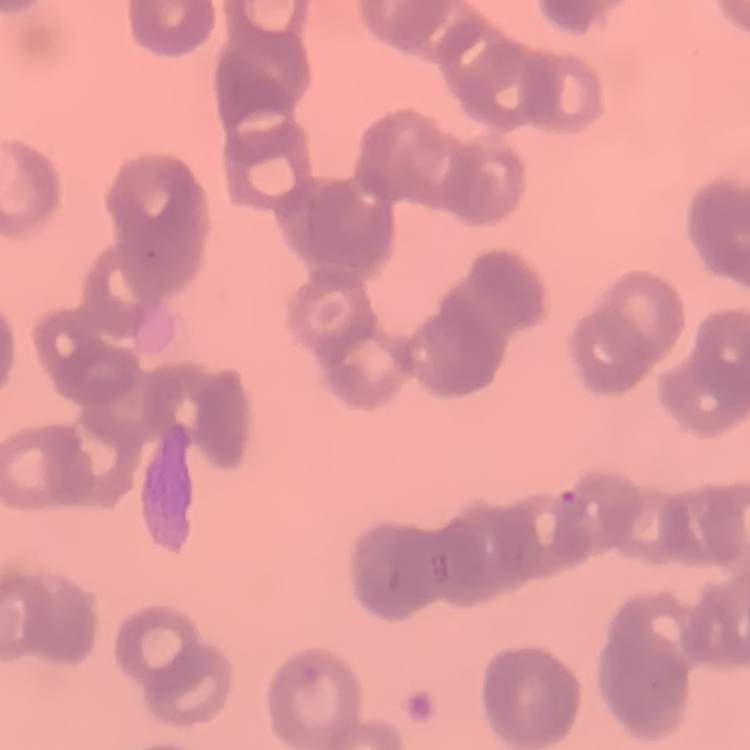

The red blood cells exhibit rouleaux formation. Field's or Giemsa stain. Thin blood film. Square crop of a larger photomicrograph.